State which cell type is depicted.
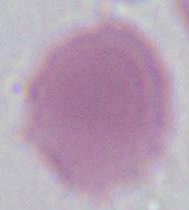
This is an erythrocyte.

Summary:
  - Magnification: 1000x
  - Modality: photomicrograph